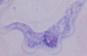

Summary:
  - Magnification: 1000x
  - Modality: photomicrograph
  - Identification: trypanosome